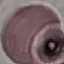

Malaria status: uninfected. Automatically extracted cell patch, resized to 64 × 64 pixels. Giemsa stain. Acquired by smartphone through the microscope eyepiece. Thin blood smear.